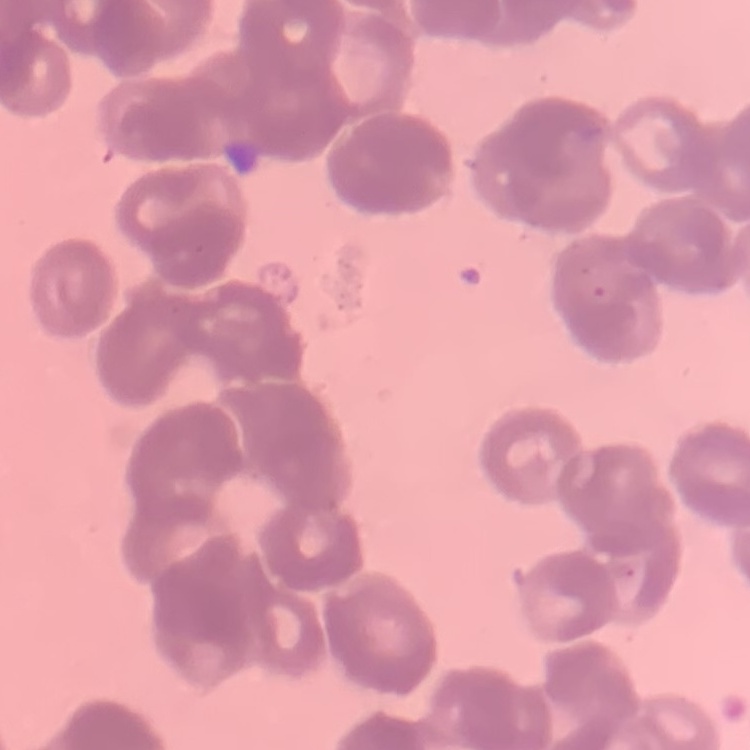

The red blood cells exhibit rouleaux formation. Field's or Giemsa stain. Thin peripheral smear. One tile cut from a larger photomicrograph.